Locate every blood parasite and identify its species.
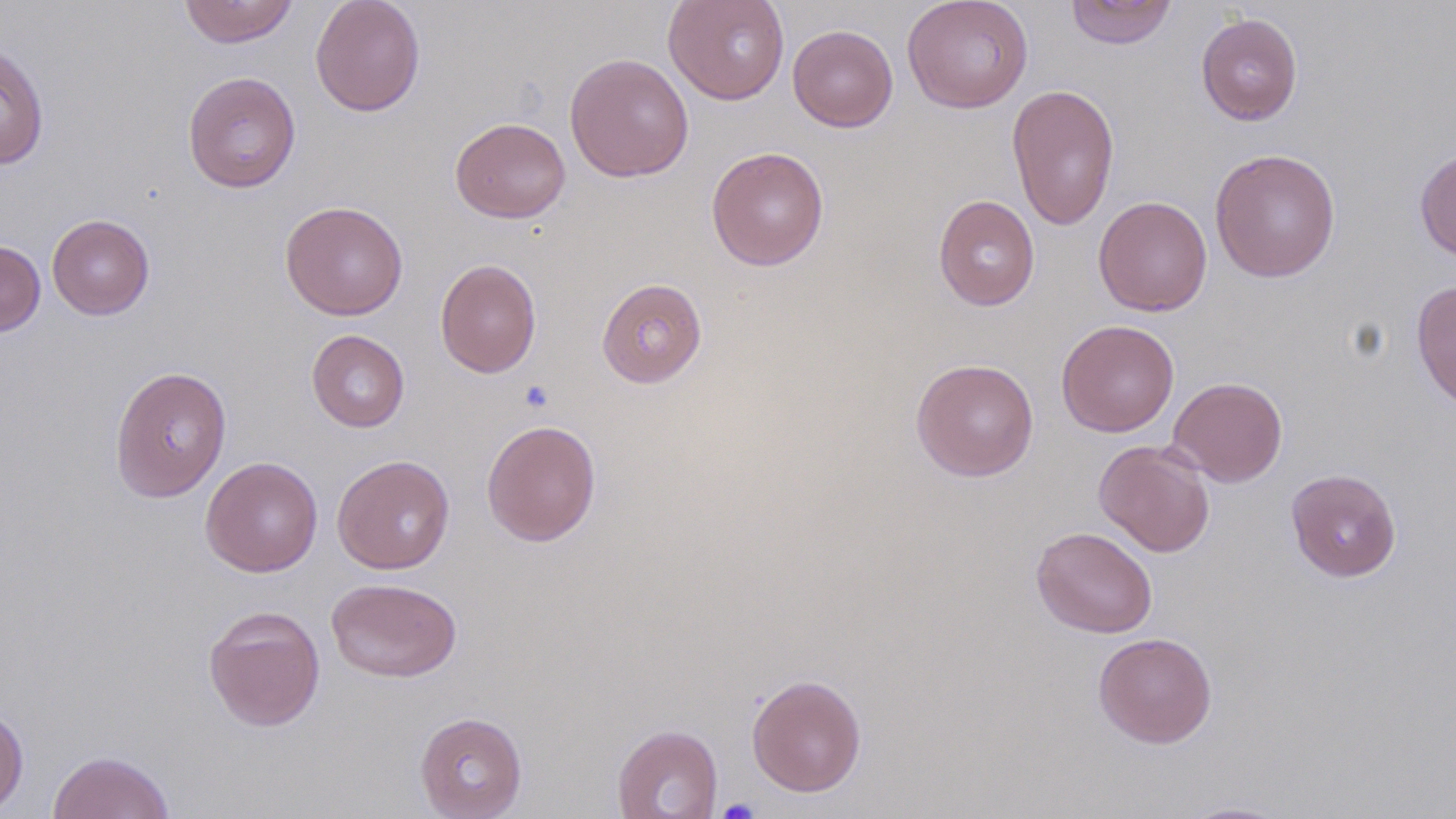

No blood parasites observed.

slide-level diagnosis = negative for blood parasites
stain = May-Grünwald-Giemsa
platelet locations = approximate bounding boxes as (x1,y1)-(x2,y2) corner pairs in pixels: (519,380)-(554,412), (716,798)-(759,819)
field of view = one of a larger specimen
modality = light microscopy
uninfected red blood cell locations = approximate bounding boxes as (x1,y1)-(x2,y2) corner pairs in pixels: (178,0)-(299,48), (310,0)-(426,116), (663,0)-(790,105), (902,0)-(1033,113), (1065,0)-(1178,49), (1195,12)-(1303,125), (787,24)-(898,132), (0,41)-(49,170), (564,52)-(694,182), (183,70)-(301,193), (1007,83)-(1120,232), (449,117)-(571,223), (706,146)-(829,271), (1209,148)-(1341,282), (1414,149)-(1456,262), (933,194)-(1040,311), (1093,196)-(1213,316), (279,200)-(408,321), (47,214)-(155,320), (0,240)-(45,337), (435,258)-(542,378), (596,277)-(707,388), (1411,278)-(1456,412), (1056,319)-(1179,437), (307,330)-(410,432), (910,358)-(1040,482), (109,366)-(233,502), (1168,376)-(1288,487), (481,419)-(602,546), (1094,440)-(1215,557), (332,454)-(455,574), (200,456)-(323,577), (1286,468)-(1402,582), (1031,525)-(1158,638), (327,577)-(462,682), (203,604)-(326,732), (1093,632)-(1217,748), (746,673)-(867,797), (0,705)-(29,815), (414,711)-(527,818), (611,724)-(723,819), (47,749)-(176,819), (1177,801)-(1295,818)
magnification = 1000x
preparation = thin blood smear
image size = 1456×819 pixels